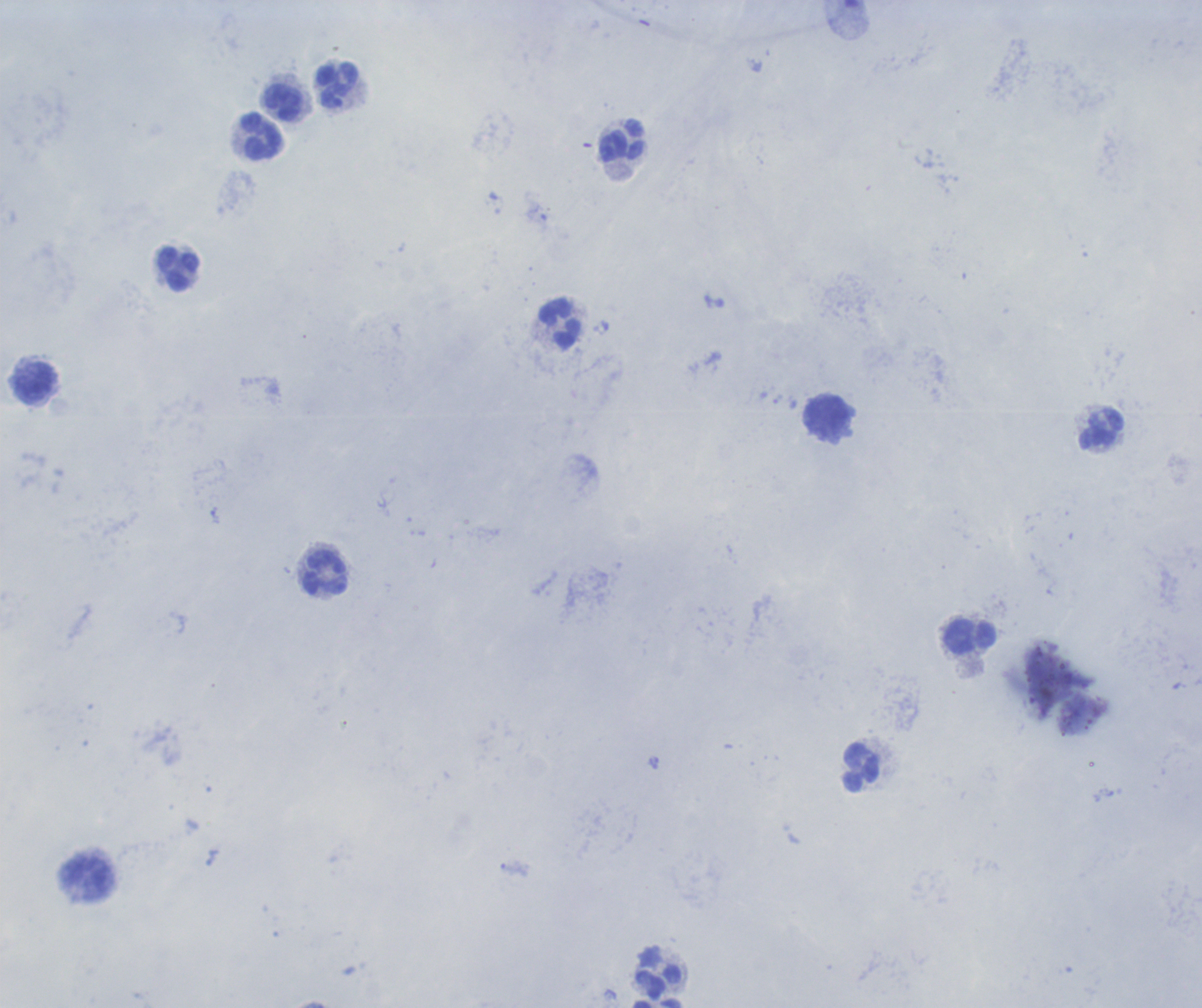

coordinate format = approximate centers as (x, y) in pixels
leukocyte locations = (338, 84), (284, 103), (262, 136), (623, 140), (177, 269), (559, 324), (35, 382), (826, 417), (1101, 429), (325, 573), (970, 636), (861, 767), (658, 972)
stain = Romanowsky
image size = 1202×1008 pixels
preparation = thick blood smear
result = no malaria parasites seen
magnification = 100x
background quality = poor
field of view = single
context = previously used in a real diagnosis